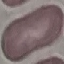
result = no malaria parasites detected
stain = Giemsa
capture = smartphone through the microscope eyepiece
preparation = thin smear
image type = cell patch, automatically extracted from a larger field of view and resized to 64 × 64 pixels